Name the parasite shown.
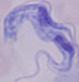
A trypanosome.

modality: micrograph
magnification: 1000x